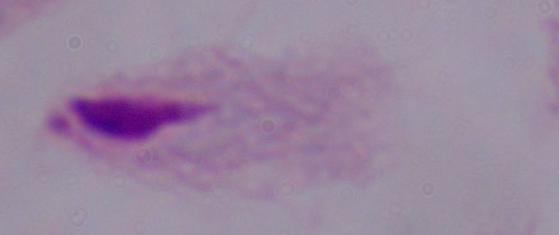
{
  "modality": "photomicrograph",
  "identification": "trichomonad",
  "magnification": "1000x"
}